Describe the morphology of the erythrocytes.
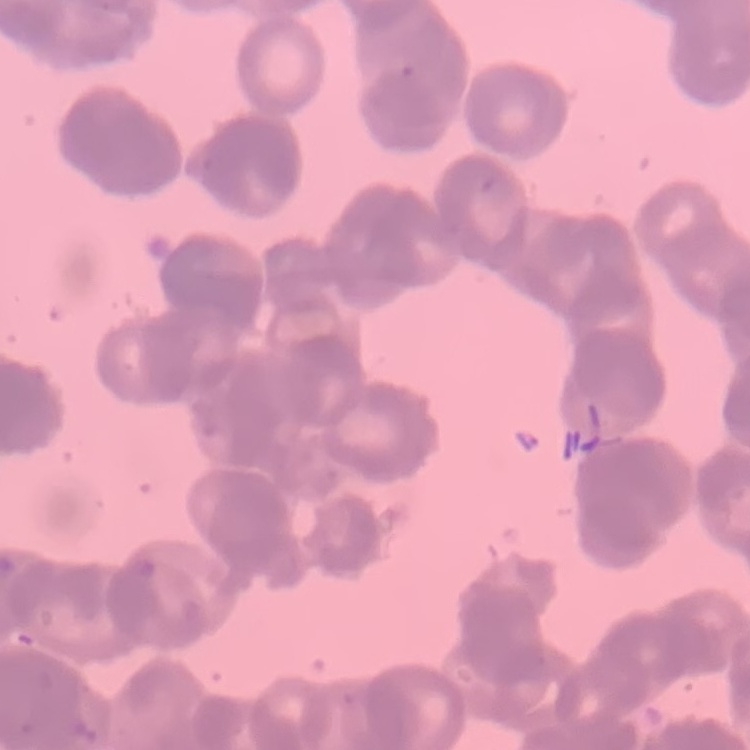
Rouleaux formation.

Summary:
  - Preparation: thin peripheral smear
  - Image type: one tile cut from a larger photomicrograph
  - Stain: Field's or Giemsa